Point out each Plasmodium parasite.
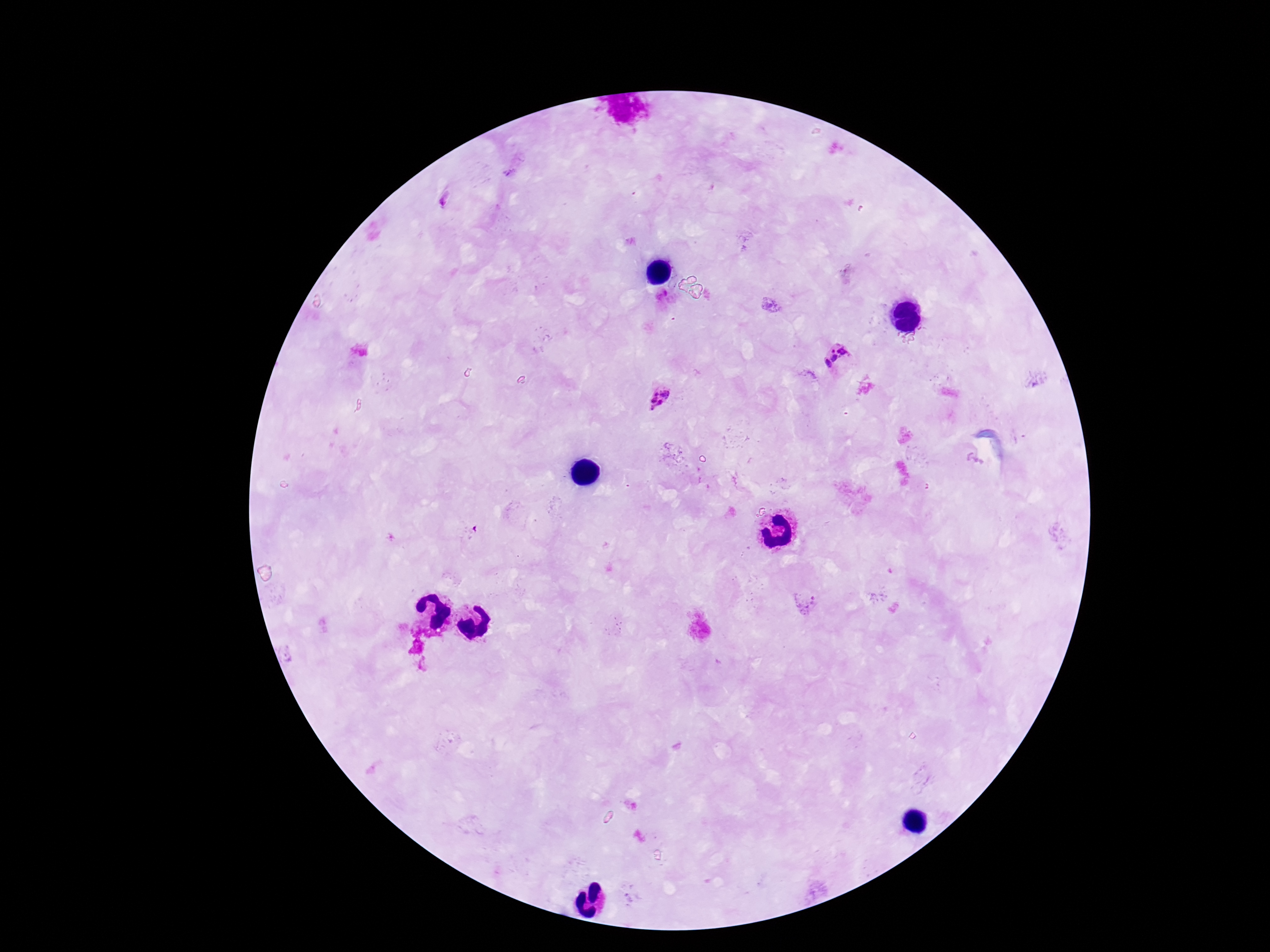

Approximate centers as (x, y) in pixels.
Plasmodium parasites: (837, 356), (659, 397).

Patient malaria status: positive. 100x magnification. Single field of view. Giemsa-stained preparation. Image is 1270×952 pixels. Thick blood smear. Smartphone photograph taken through the microscope eyepiece.